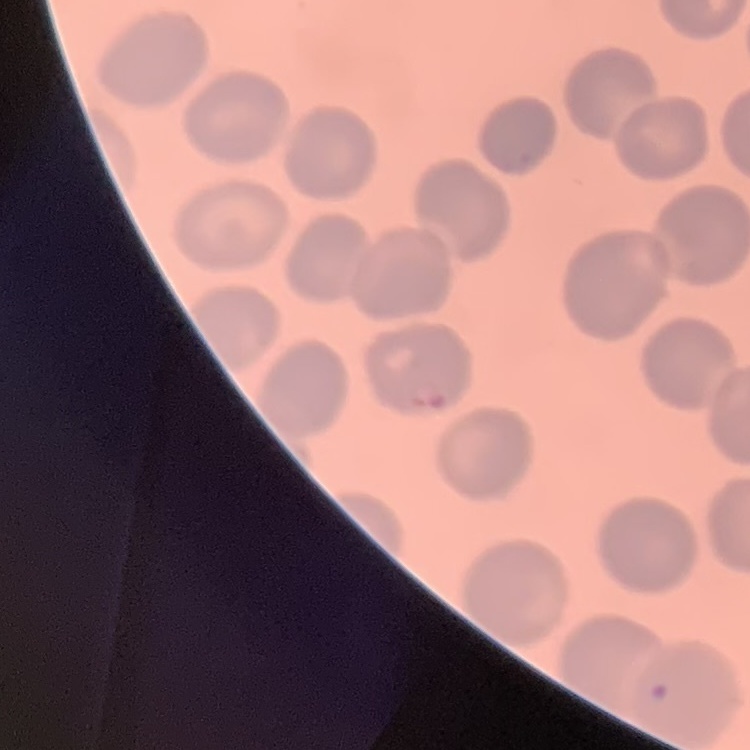
red_blood_cell_morphology: no rouleaux formation
image_type: square crop of a larger photomicrograph
preparation: thin blood film
stain: Field's or Giemsa